Give the position of every Plasmodium parasite visible.
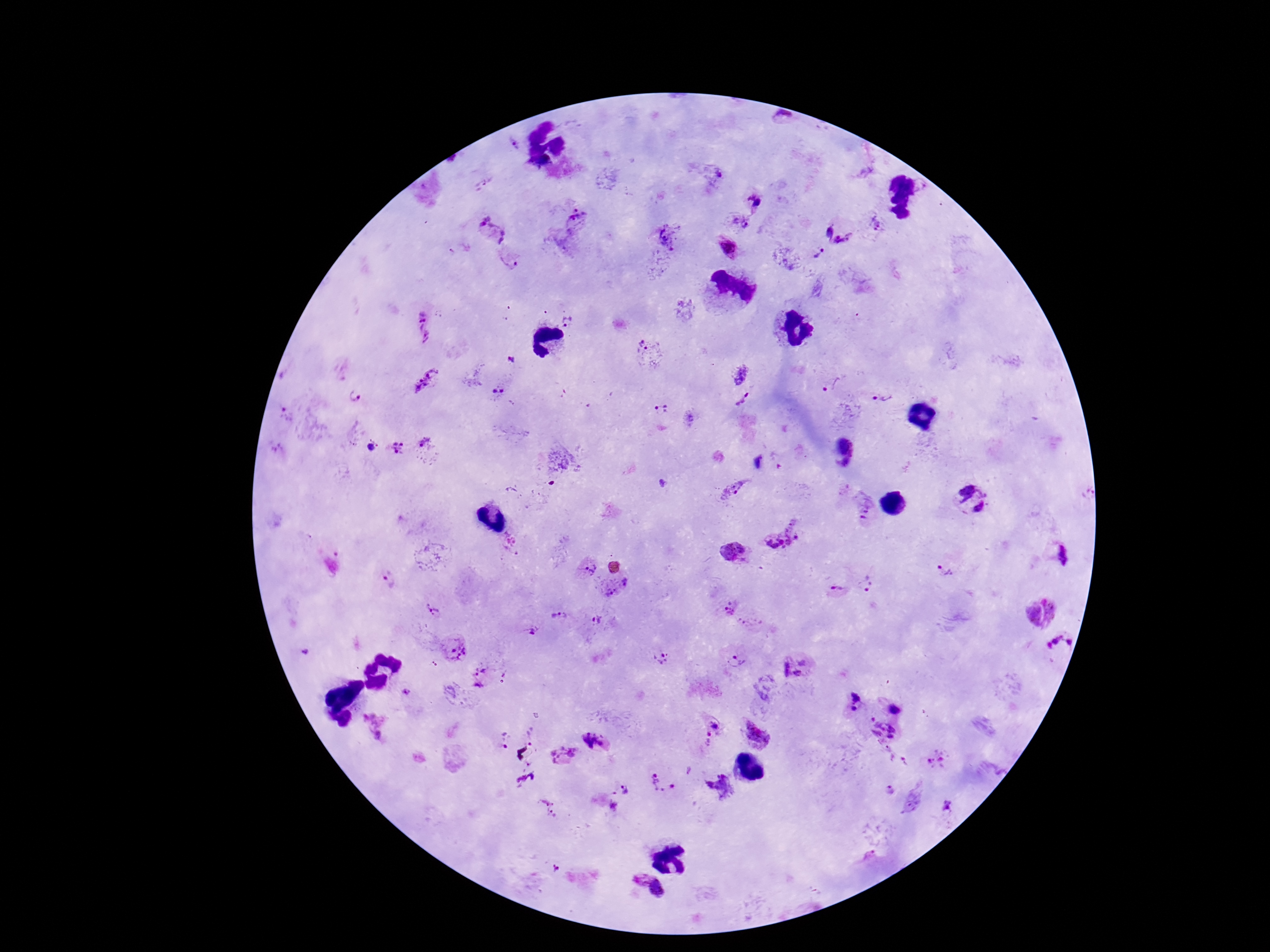

Approximate centers as (x, y) in pixels.
Plasmodium parasites: (513, 143), (710, 172), (484, 184), (756, 202), (733, 221), (875, 223), (567, 226), (491, 230), (826, 230), (662, 241), (842, 242), (458, 251), (819, 254), (509, 262), (568, 320), (424, 327), (648, 350), (510, 359), (741, 374), (424, 378), (832, 385), (501, 391), (355, 396), (881, 398), (744, 400), (662, 410), (423, 445), (371, 447), (397, 449), (663, 483), (733, 489), (970, 499), (863, 507), (783, 535), (512, 542), (736, 552), (1058, 555), (587, 567), (951, 571), (391, 579), (867, 585), (616, 589), (838, 592), (726, 609), (431, 610), (1038, 613), (558, 616), (597, 620), (752, 625), (533, 632), (453, 647), (1060, 647), (660, 658), (735, 660), (796, 667), (483, 676), (403, 691), (852, 703), (896, 708), (373, 724), (707, 733), (756, 734), (882, 734), (530, 737), (504, 742), (595, 742), (563, 755), (936, 760), (527, 775), (662, 781), (719, 788), (887, 790), (627, 791), (912, 800), (613, 803), (948, 805), (548, 807), (871, 856), (551, 869), (645, 892).

Thick blood smear. Giemsa stain. Photographed through the microscope eyepiece with a smartphone camera. Image is 1270×952 pixels. Patient malaria status: positive. Single field of view. 100x magnification.